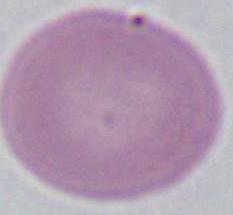
identification = erythrocyte
modality = micrograph
magnification = 1000x